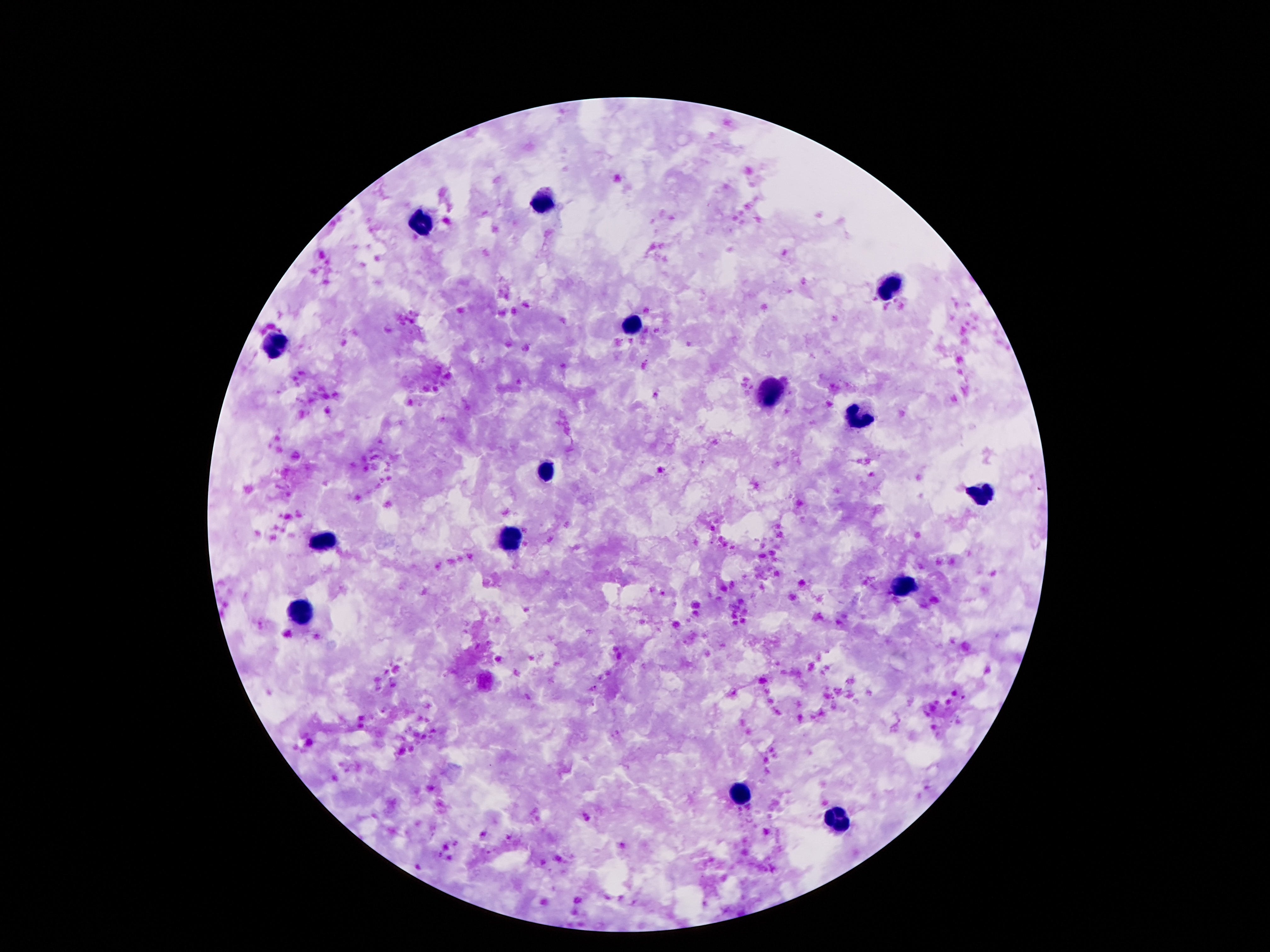
Approximate centers as {x, y} in pixels.
Summary:
  - Leukocyte locations: {548, 198}, {419, 220}, {886, 289}, {630, 325}, {272, 347}, {768, 392}, {861, 418}, {546, 474}, {977, 493}, {511, 543}, {324, 545}, {904, 589}, {302, 616}, {738, 796}, {835, 823}
  - Stain: Giemsa
  - Field of view: single
  - Capture: smartphone camera through the microscope eyepiece
  - Patient malaria status: negative
  - Image size: 1270×952 pixels
  - Magnification: 100x
  - Preparation: thick blood smear